Assess this cell for malaria.
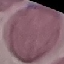
Uninfected.

image type = cell patch, automatically extracted from a larger field of view and resized to 64 × 64 pixels
stain = Giemsa
capture = smartphone through the microscope eyepiece
preparation = thin blood smear